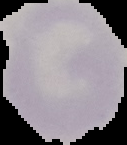
image_type: segmented cell region on a black background
result: no malaria parasites seen
image_size: 127×145 pixels
preparation: thin blood film